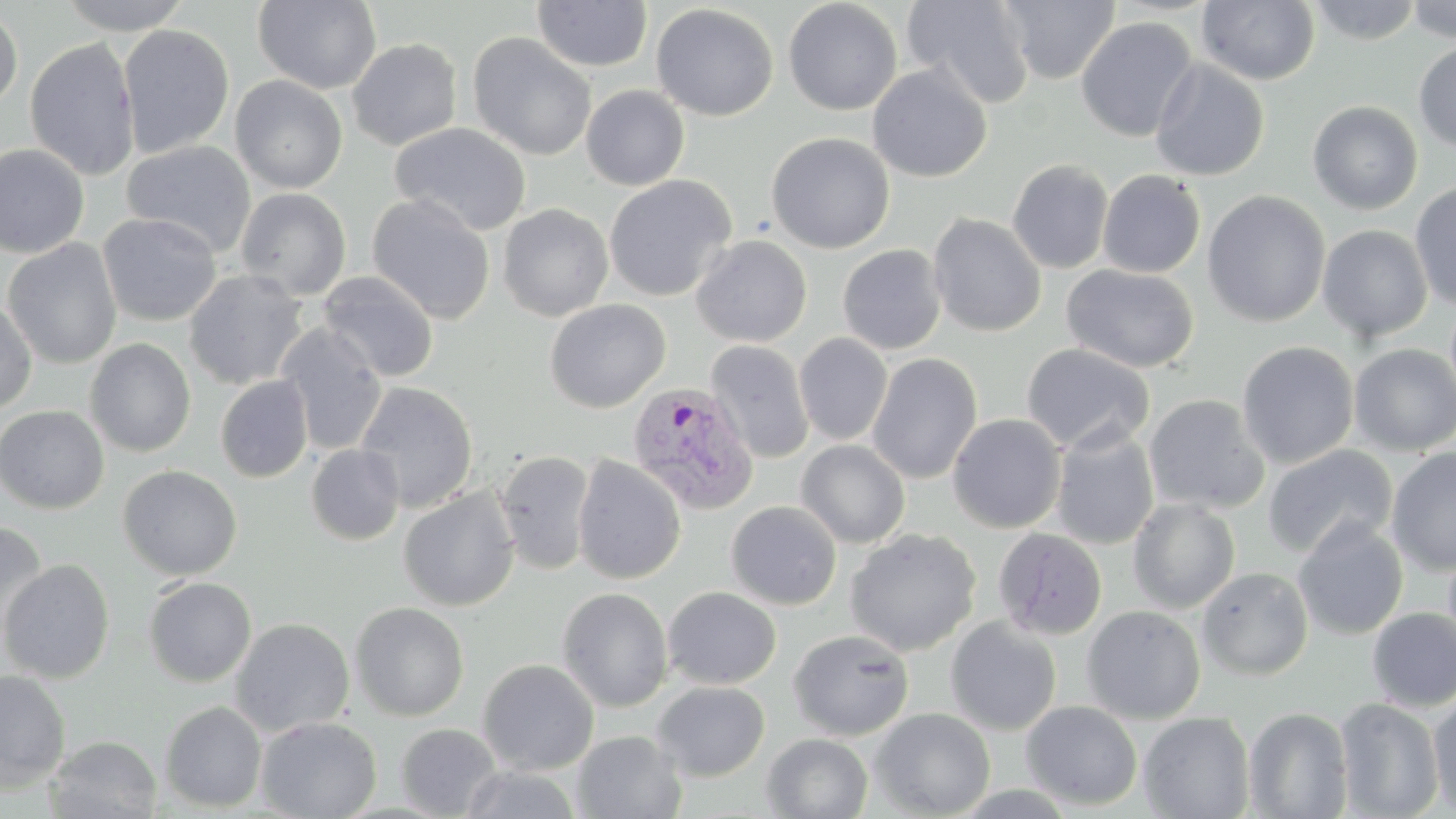

Approximate bounding boxes as (x1, y1, x2, y2) in pixels. Uninfected red blood cell locations: (57, 0, 195, 34), (253, 0, 382, 94), (532, 0, 653, 72), (783, 0, 903, 116), (902, 0, 1036, 108), (999, 0, 1120, 84), (1197, 0, 1320, 85), (1307, 0, 1423, 45), (1404, 0, 1456, 42), (651, 4, 779, 121), (0, 7, 23, 114), (1076, 17, 1198, 142), (118, 24, 235, 159), (466, 32, 597, 161), (24, 37, 139, 180), (346, 38, 463, 151), (1414, 40, 1456, 153), (1149, 59, 1270, 181), (867, 64, 992, 182), (230, 75, 348, 194), (581, 85, 690, 191), (1307, 100, 1423, 215), (390, 122, 531, 236), (766, 132, 895, 254), (121, 140, 257, 258), (0, 143, 90, 259), (1007, 159, 1114, 273), (1097, 169, 1206, 278), (603, 174, 738, 302), (1409, 182, 1456, 310), (235, 187, 352, 300), (1202, 190, 1331, 327), (367, 193, 495, 325), (497, 203, 614, 321), (97, 212, 222, 326), (927, 213, 1047, 337), (1317, 225, 1432, 342), (691, 235, 811, 347), (2, 238, 122, 369), (837, 244, 947, 355), (1062, 264, 1199, 373), (184, 270, 308, 390), (317, 271, 439, 383), (0, 297, 37, 413), (545, 298, 670, 413), (275, 323, 387, 455), (794, 333, 893, 446), (84, 338, 196, 457), (705, 340, 814, 464), (1236, 341, 1359, 469), (1021, 343, 1155, 455), (1349, 344, 1456, 456), (866, 352, 982, 485), (216, 375, 313, 482), (354, 381, 479, 513), (1144, 394, 1269, 513), (0, 405, 108, 514), (947, 414, 1067, 534), (1050, 425, 1159, 550), (796, 440, 910, 549), (306, 443, 404, 545), (1262, 445, 1398, 560), (1386, 447, 1456, 576), (494, 450, 596, 577), (572, 454, 686, 585), (118, 465, 242, 580), (398, 487, 520, 611), (1128, 497, 1240, 614), (725, 500, 842, 610), (1293, 518, 1409, 640), (0, 522, 47, 644), (844, 528, 981, 657), (992, 528, 1108, 640), (1, 559, 115, 684), (1196, 566, 1313, 680), (143, 577, 256, 687), (556, 587, 674, 712), (662, 587, 781, 689), (349, 601, 469, 721), (1081, 605, 1206, 724), (1367, 607, 1456, 711), (945, 617, 1062, 735), (230, 618, 355, 736), (788, 629, 914, 741), (477, 658, 599, 775), (0, 669, 71, 792), (652, 681, 770, 781), (1428, 692, 1456, 816), (1335, 698, 1445, 818), (160, 701, 267, 812), (1021, 701, 1143, 810), (1244, 707, 1353, 818), (869, 708, 995, 818), (1139, 712, 1254, 818), (256, 716, 382, 818), (396, 724, 501, 817), (572, 730, 687, 818), (762, 733, 873, 818), (46, 735, 162, 818), (458, 766, 584, 819). Plasmodium vivax-infected red blood cell locations: (627, 382, 759, 514). Slide-level diagnosis: Plasmodium vivax. May-Grünwald-Giemsa-stained preparation. 1000x magnification. Optical microscopy. Image is 1456×819 pixels. Thin blood film. Single field of view.